Locate and identify every blood parasite.
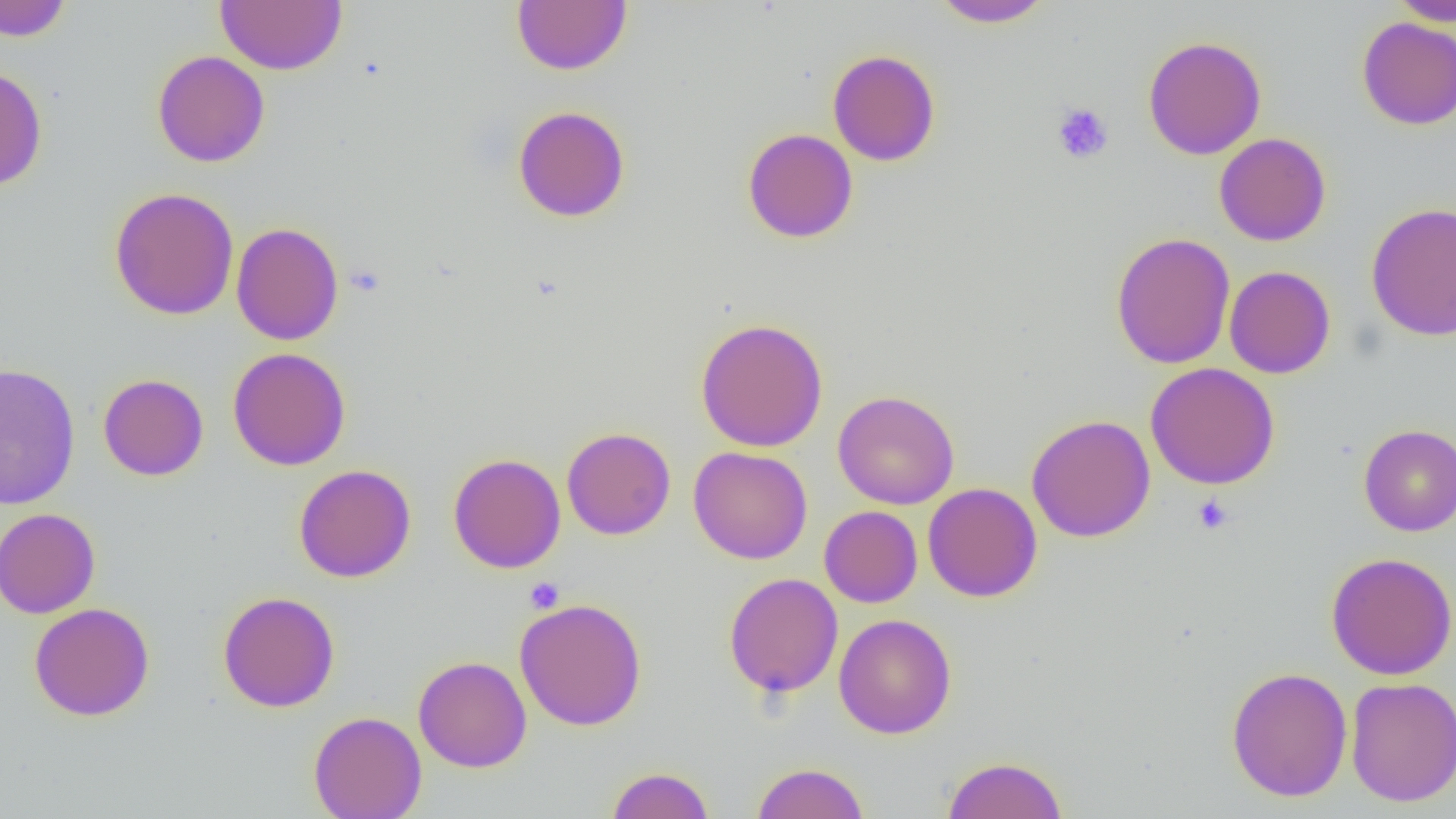

No blood parasites observed.

Summary:
  - Coordinate format: approximate bounding boxes as [x1, y1, x2, y2] in pixels
  - Platelet locations: [1051, 102, 1114, 165], [1192, 494, 1234, 535], [524, 577, 564, 614]
  - Uninfected red blood cell locations: [0, 0, 72, 41], [512, 0, 631, 75], [930, 0, 1056, 28], [1388, 0, 1456, 26], [215, 1, 347, 74], [1357, 17, 1456, 130], [1142, 36, 1267, 160], [827, 49, 941, 166], [152, 50, 270, 168], [0, 66, 47, 192], [513, 105, 630, 222], [742, 128, 858, 243], [1214, 133, 1331, 246], [109, 187, 240, 320], [1365, 202, 1456, 341], [230, 222, 344, 346], [1110, 232, 1235, 369], [1224, 265, 1336, 378], [695, 317, 829, 452], [228, 347, 351, 471], [1145, 362, 1280, 489], [0, 363, 80, 510], [98, 373, 209, 481], [832, 390, 960, 509], [1026, 414, 1156, 542], [1358, 424, 1456, 536], [561, 426, 676, 540], [688, 447, 812, 564], [448, 453, 566, 573], [293, 464, 416, 582], [922, 482, 1042, 602], [819, 505, 922, 608], [0, 508, 100, 618], [1326, 552, 1456, 679], [723, 572, 843, 698], [218, 591, 340, 712], [514, 596, 648, 732], [29, 602, 155, 722], [833, 613, 957, 739], [413, 656, 532, 773], [1225, 666, 1353, 802], [1345, 677, 1456, 807], [308, 711, 427, 819], [942, 755, 1068, 818], [750, 761, 870, 819], [605, 766, 715, 819]
  - Slide-level diagnosis: no evidence of blood parasites
  - Field of view: single
  - Modality: light microscopy
  - Magnification: 1000x
  - Preparation: thin blood smear
  - Image size: 1456×819 pixels